Name the parasite shown.
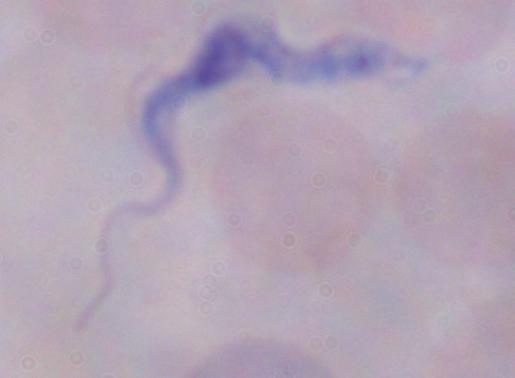
A trypanosome.

modality: micrograph
magnification: 1000x